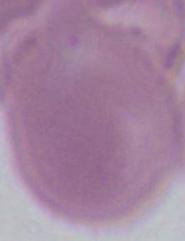

{
  "modality": "photomicrograph",
  "identification": "erythrocyte",
  "magnification": "1000x"
}